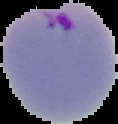 Image is 118×124 pixels. Result: malaria parasites identified. From a thin blood smear. The area outside the segmented cell region is set to black.